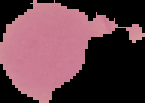

Summary:
  - Image size: 145×103 pixels
  - Preparation: thin blood smear
  - Image type: segmented cell region on a black background
  - Malaria status: uninfected